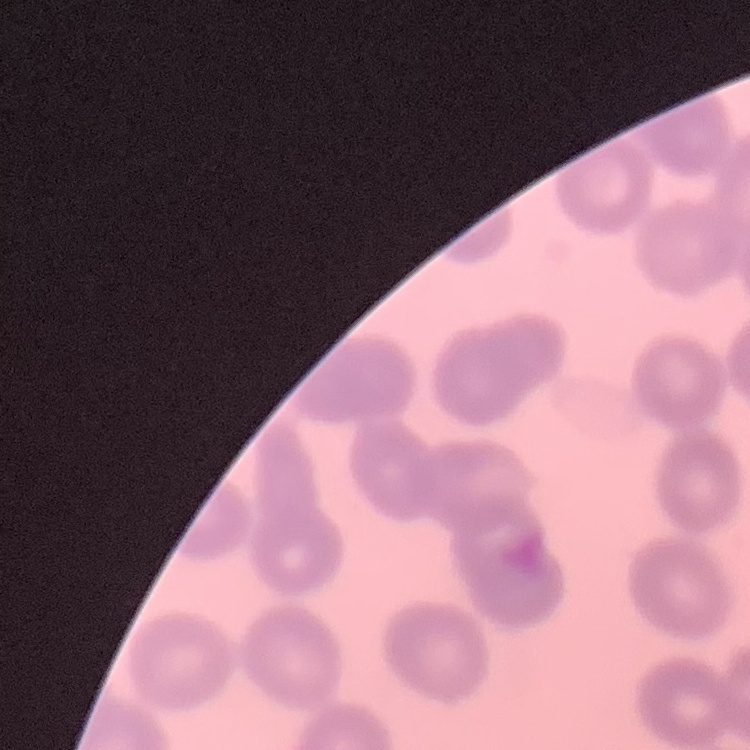
erythrocyte morphology = no rouleaux formation
image type = one tile cut from a larger photomicrograph
preparation = thin peripheral smear
stain = Field's or Giemsa